Assess this cell for malaria.
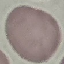
It is uninfected.

Thin blood smear. Giemsa stain. Acquired by smartphone through the microscope eyepiece. Automatically extracted cell patch, resized to 64 × 64 pixels.